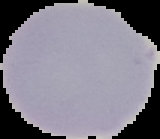 Image is 160×139 pixels. Result: no Plasmodium parasites detected. From a thin blood smear. Cell region segmented out of the field of view; the surrounding area is masked to black.